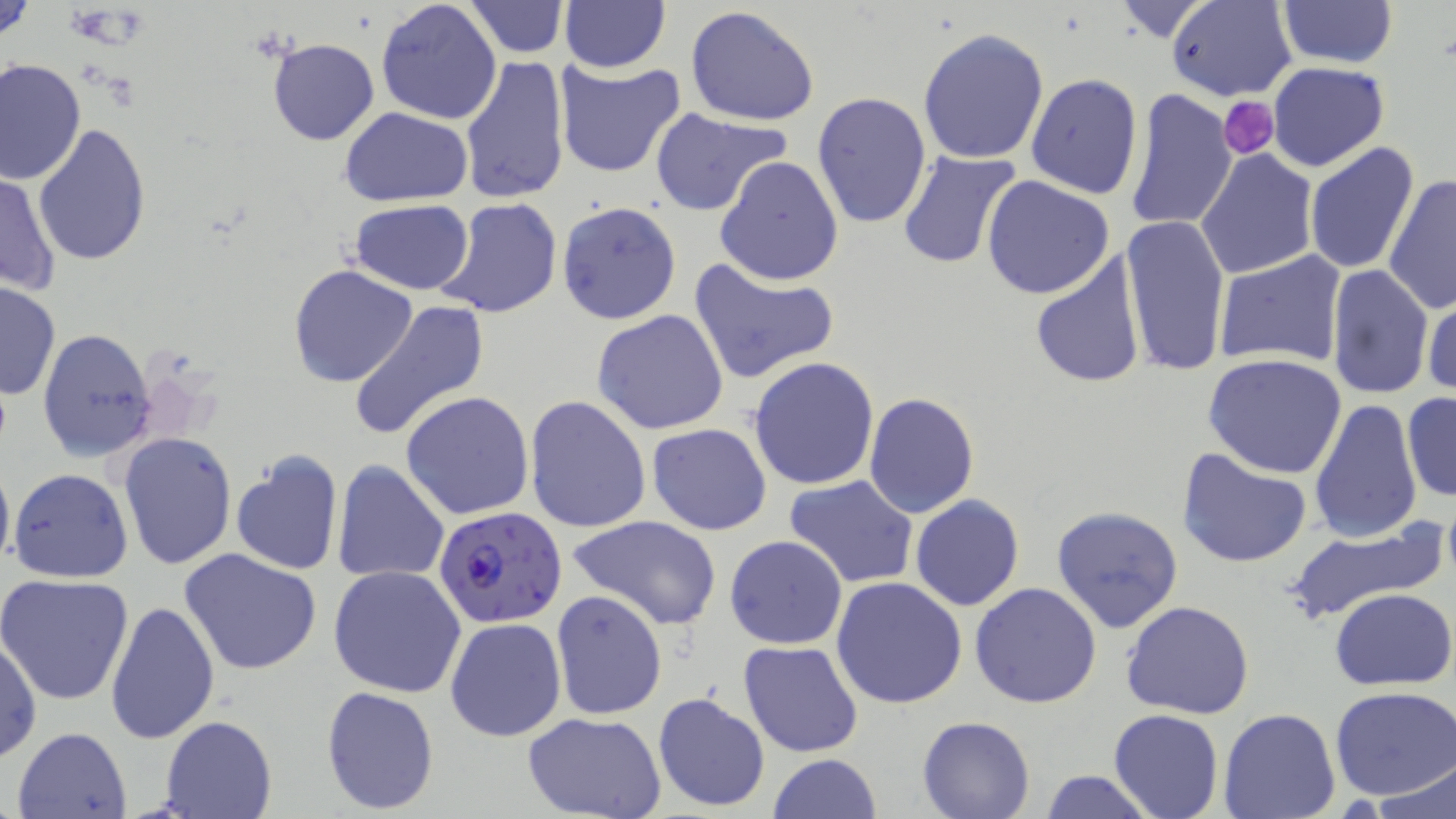
{
  "slide_level_diagnosis": "Plasmodium falciparum",
  "image_size": "1456×819 pixels",
  "platelet_locations": "approximate bounding boxes as (x1, y1, x2, y2) in pixels: (66, 5, 131, 46), (1218, 97, 1281, 157)",
  "stain": "May-Grünwald-Giemsa",
  "plasmodium_falciparum_infected_red_blood_cell_locations": "approximate bounding boxes as (x1, y1, x2, y2) in pixels: (433, 507, 568, 629)",
  "magnification": "1000x",
  "uninfected_red_blood_cell_locations": "approximate bounding boxes as (x1, y1, x2, y2) in pixels: (1, 0, 37, 47), (1167, 0, 1296, 101), (375, 1, 503, 125), (463, 1, 568, 57), (1277, 1, 1398, 69), (557, 2, 671, 73), (1111, 2, 1218, 43), (686, 6, 820, 127), (916, 26, 1049, 164), (266, 37, 378, 145), (458, 54, 569, 205), (1, 59, 86, 187), (553, 59, 684, 177), (1267, 62, 1390, 172), (1026, 72, 1144, 198), (1126, 90, 1236, 233), (810, 91, 931, 229), (340, 108, 476, 206), (649, 108, 791, 216), (33, 125, 152, 267), (1304, 141, 1421, 274), (897, 149, 1025, 270), (1197, 149, 1319, 279), (714, 155, 843, 286), (0, 171, 61, 296), (1383, 173, 1456, 315), (982, 175, 1115, 299), (435, 197, 564, 319), (348, 200, 474, 294), (557, 201, 682, 324), (1121, 213, 1229, 379), (1212, 249, 1347, 369), (1028, 252, 1147, 390), (688, 256, 840, 385), (1325, 263, 1433, 401), (288, 264, 419, 387), (0, 281, 60, 400), (1422, 289, 1455, 403), (348, 300, 490, 442), (592, 308, 729, 435), (37, 328, 155, 462), (1203, 352, 1351, 479), (749, 357, 880, 489), (400, 392, 535, 521), (863, 392, 979, 518), (1402, 392, 1456, 505), (525, 395, 651, 533), (1309, 398, 1423, 546), (646, 422, 772, 535), (118, 431, 237, 570), (1177, 446, 1312, 570), (229, 447, 343, 574), (0, 453, 14, 577), (332, 459, 451, 585), (9, 467, 133, 583), (783, 474, 919, 590), (910, 495, 1025, 612), (1050, 505, 1183, 633), (566, 513, 722, 632), (1286, 521, 1445, 626), (724, 535, 848, 649), (179, 548, 323, 678), (328, 565, 466, 699), (0, 573, 134, 704), (831, 576, 967, 708), (969, 582, 1102, 708), (1329, 587, 1455, 691), (551, 589, 667, 719), (105, 599, 219, 744), (1121, 600, 1254, 720), (443, 616, 566, 742), (0, 630, 42, 765), (738, 639, 863, 759), (319, 684, 440, 815), (1330, 686, 1456, 802), (652, 689, 771, 813), (1218, 708, 1341, 819), (1109, 709, 1224, 819), (524, 713, 666, 819), (917, 715, 1036, 819), (159, 716, 276, 819), (12, 725, 132, 818), (768, 754, 881, 818), (1374, 763, 1456, 818), (1042, 770, 1157, 818)",
  "preparation": "thin blood smear",
  "modality": "optical microscopy",
  "field_of_view": "single"
}